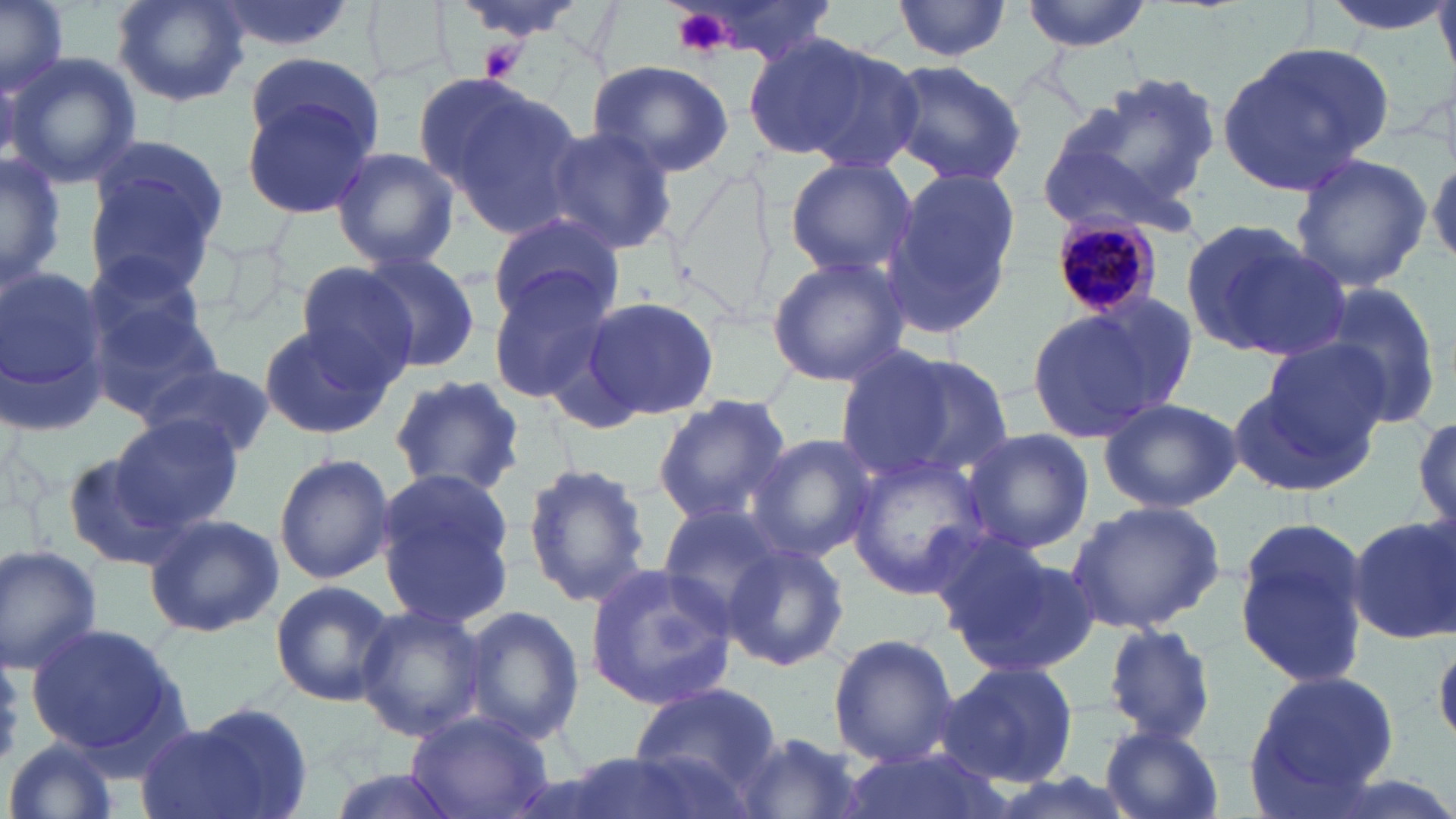

slide-level diagnosis = Plasmodium malariae
field of view = single
uninfected red blood cell locations = approximate bounding boxes as named x1/y1/x2/y2 corners in pixels: (x1=0, y1=0, x2=73, y2=99), (x1=111, y1=0, x2=250, y2=107), (x1=207, y1=0, x2=359, y2=53), (x1=445, y1=0, x2=602, y2=41), (x1=665, y1=0, x2=846, y2=68), (x1=892, y1=0, x2=1015, y2=61), (x1=1019, y1=0, x2=1154, y2=52), (x1=1316, y1=0, x2=1455, y2=36), (x1=745, y1=32, x2=910, y2=167), (x1=1218, y1=41, x2=1394, y2=192), (x1=242, y1=50, x2=385, y2=169), (x1=5, y1=54, x2=143, y2=188), (x1=586, y1=59, x2=735, y2=178), (x1=881, y1=59, x2=1027, y2=188), (x1=1048, y1=71, x2=1222, y2=228), (x1=424, y1=76, x2=588, y2=233), (x1=239, y1=90, x2=380, y2=221), (x1=540, y1=124, x2=679, y2=256), (x1=83, y1=140, x2=227, y2=286), (x1=329, y1=145, x2=459, y2=272), (x1=0, y1=151, x2=66, y2=290), (x1=1287, y1=153, x2=1434, y2=292), (x1=1428, y1=156, x2=1456, y2=265), (x1=783, y1=157, x2=919, y2=283), (x1=885, y1=169, x2=1023, y2=337), (x1=485, y1=211, x2=623, y2=325), (x1=1179, y1=217, x2=1345, y2=365), (x1=80, y1=252, x2=220, y2=381), (x1=356, y1=252, x2=481, y2=374), (x1=765, y1=253, x2=911, y2=387), (x1=295, y1=262, x2=418, y2=385), (x1=0, y1=266, x2=112, y2=434), (x1=486, y1=268, x2=616, y2=412), (x1=1314, y1=282, x2=1445, y2=430), (x1=1076, y1=289, x2=1200, y2=419), (x1=582, y1=295, x2=720, y2=421), (x1=88, y1=304, x2=223, y2=423), (x1=1021, y1=307, x2=1169, y2=444), (x1=256, y1=321, x2=395, y2=439), (x1=1255, y1=336, x2=1390, y2=460), (x1=836, y1=347, x2=1011, y2=487), (x1=146, y1=364, x2=274, y2=460), (x1=1227, y1=372, x2=1377, y2=498), (x1=391, y1=374, x2=525, y2=498), (x1=651, y1=395, x2=793, y2=527), (x1=1098, y1=397, x2=1242, y2=513), (x1=1411, y1=413, x2=1455, y2=534), (x1=110, y1=414, x2=245, y2=533), (x1=960, y1=427, x2=1095, y2=555), (x1=746, y1=432, x2=881, y2=564), (x1=845, y1=450, x2=996, y2=598), (x1=62, y1=452, x2=192, y2=573), (x1=273, y1=453, x2=395, y2=585), (x1=520, y1=460, x2=653, y2=610), (x1=372, y1=469, x2=520, y2=633), (x1=1066, y1=499, x2=1226, y2=634), (x1=655, y1=506, x2=783, y2=624), (x1=142, y1=512, x2=286, y2=638), (x1=1232, y1=513, x2=1374, y2=690), (x1=1345, y1=514, x2=1456, y2=645), (x1=720, y1=539, x2=851, y2=673), (x1=940, y1=541, x2=1100, y2=680), (x1=0, y1=545, x2=104, y2=673), (x1=584, y1=563, x2=738, y2=711), (x1=270, y1=579, x2=395, y2=707), (x1=353, y1=604, x2=490, y2=743), (x1=461, y1=606, x2=585, y2=745), (x1=1099, y1=622, x2=1222, y2=745), (x1=22, y1=623, x2=185, y2=761), (x1=828, y1=632, x2=959, y2=768), (x1=938, y1=659, x2=1082, y2=791), (x1=1245, y1=667, x2=1402, y2=812), (x1=627, y1=682, x2=782, y2=791), (x1=152, y1=703, x2=314, y2=819), (x1=406, y1=709, x2=553, y2=819), (x1=1099, y1=725, x2=1226, y2=819), (x1=730, y1=732, x2=869, y2=819), (x1=5, y1=738, x2=126, y2=819), (x1=849, y1=745, x2=1004, y2=819), (x1=321, y1=766, x2=459, y2=819)
platelet locations = approximate bounding boxes as named x1/y1/x2/y2 corners in pixels: (x1=669, y1=6, x2=731, y2=59), (x1=478, y1=38, x2=524, y2=82)
magnification = 1000x
Plasmodium malariae-infected red blood cell locations = approximate bounding boxes as named x1/y1/x2/y2 corners in pixels: (x1=1055, y1=209, x2=1162, y2=330)
modality = optical microscopy
image size = 1456×819 pixels
preparation = thin blood film
stain = May-Grünwald-Giemsa